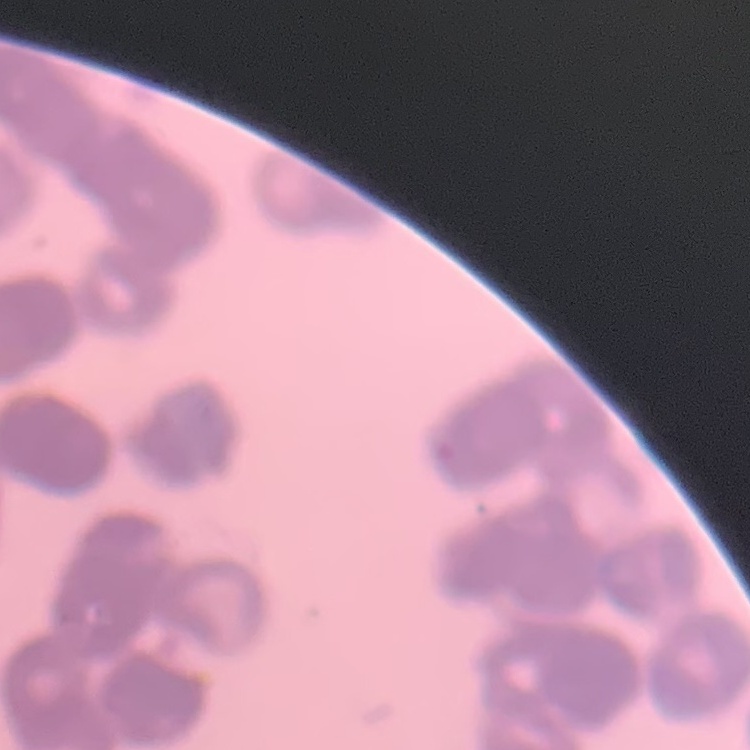
The erythrocytes exhibit rouleaux formation. Field's or Giemsa stain. Thin peripheral smear. One tile cut from a larger photomicrograph.